Report the malaria status of this cell.
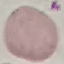

Uninfected.

Summary:
  - Preparation: thin blood film
  - Capture: smartphone camera at the microscope eyepiece
  - Image type: automatically extracted cell patch, resized to 64 × 64 pixels
  - Stain: Giemsa